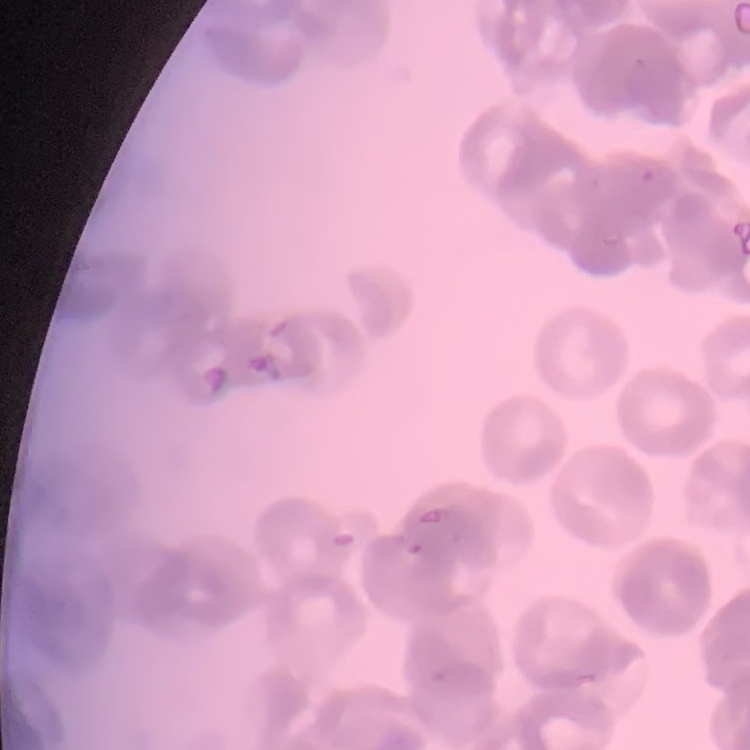

Summary:
  - Red blood cell morphology: rouleaux formation
  - Image type: square crop of a larger photomicrograph
  - Preparation: thin blood smear
  - Stain: Field's or Giemsa